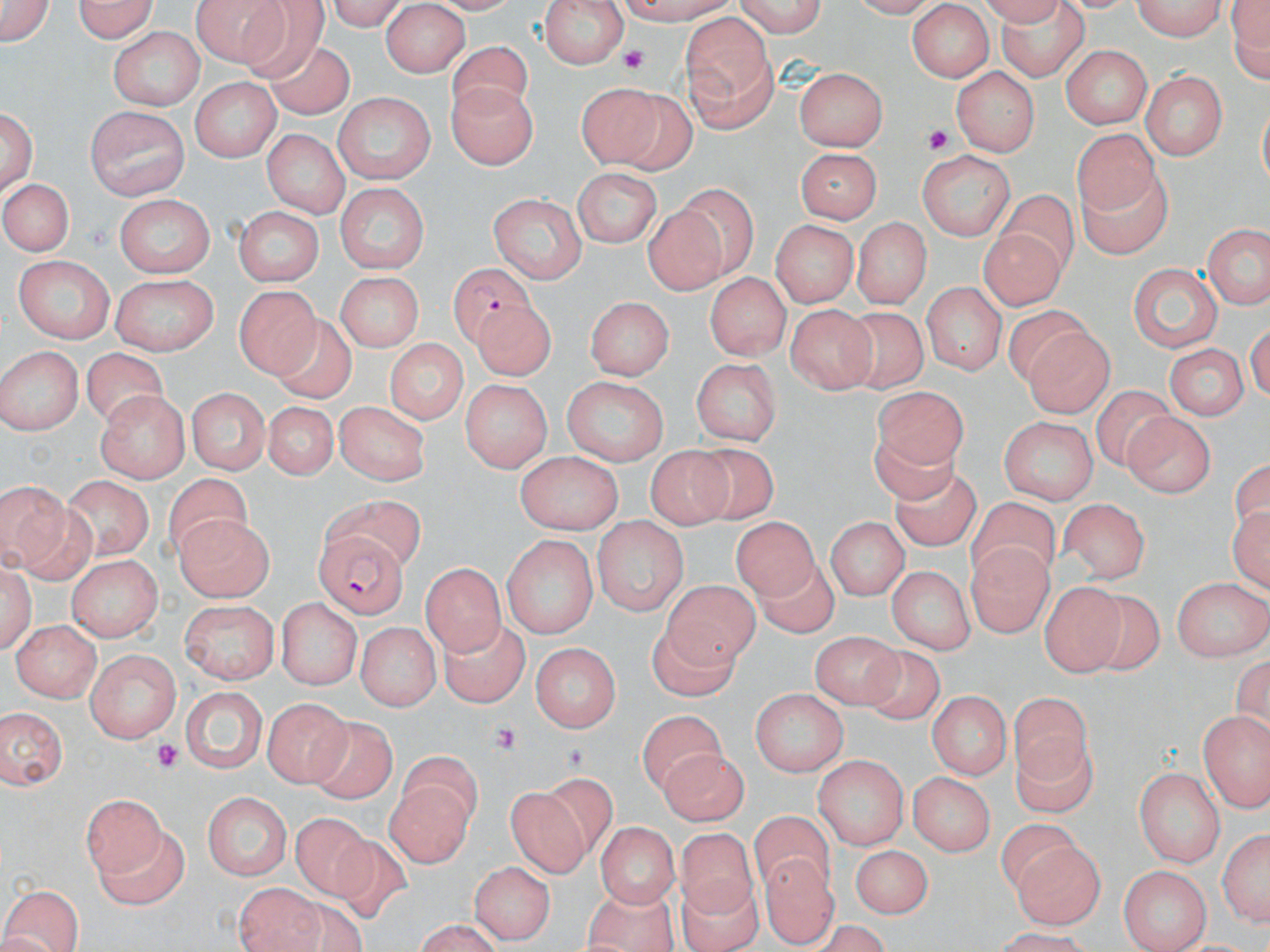 Approximate bounding boxes as [x1, y1, x2, y2] in pixels. Platelet locations: [617, 45, 659, 79], [918, 121, 953, 160], [484, 719, 520, 750], [149, 739, 186, 777]. Plasmodium falciparum-infected red blood cell locations: [440, 263, 546, 348], [316, 531, 410, 617]. Uninfected red blood cell locations: [71, 0, 160, 42], [192, 0, 297, 67], [730, 0, 830, 36], [1129, 0, 1229, 40], [1224, 0, 1269, 93], [541, 3, 625, 70], [1, 4, 56, 49], [991, 4, 1093, 88], [382, 5, 467, 75], [908, 5, 993, 80], [237, 7, 334, 91], [680, 16, 779, 136], [109, 28, 206, 110], [445, 43, 541, 121], [1059, 44, 1151, 130], [256, 46, 368, 127], [954, 66, 1037, 157], [797, 67, 889, 152], [1140, 69, 1226, 160], [191, 80, 278, 162], [448, 80, 535, 170], [576, 85, 667, 176], [448, 86, 539, 177], [330, 94, 436, 188], [616, 95, 708, 182], [1, 103, 39, 202], [87, 106, 187, 203], [1064, 125, 1174, 214], [263, 130, 350, 216], [796, 148, 879, 224], [919, 150, 1016, 238], [1070, 167, 1175, 264], [572, 168, 663, 249], [0, 175, 72, 260], [332, 184, 430, 273], [680, 188, 764, 273], [1002, 190, 1079, 282], [492, 195, 586, 282], [112, 196, 218, 273], [231, 208, 325, 286], [649, 209, 728, 296], [850, 216, 928, 310], [770, 220, 855, 308], [1203, 223, 1269, 313], [980, 229, 1064, 312], [14, 255, 116, 341], [1125, 265, 1222, 356], [706, 270, 790, 358], [337, 271, 424, 353], [112, 274, 216, 356], [922, 278, 1002, 378], [234, 285, 324, 378], [583, 294, 672, 382], [996, 302, 1089, 387], [787, 303, 876, 391], [838, 308, 934, 393], [469, 309, 559, 378], [266, 310, 359, 404], [1025, 328, 1117, 420], [383, 336, 470, 425], [1170, 341, 1248, 423], [0, 345, 82, 436], [78, 345, 171, 426], [689, 355, 785, 447], [563, 375, 668, 465], [462, 379, 549, 472], [871, 384, 973, 473], [184, 386, 272, 473], [1092, 388, 1186, 476], [100, 393, 189, 481], [259, 399, 346, 484], [335, 401, 425, 484], [1124, 411, 1213, 497], [999, 415, 1097, 503], [869, 433, 961, 510], [683, 442, 782, 522], [648, 446, 737, 533], [516, 448, 620, 531], [67, 474, 152, 561], [164, 474, 256, 569], [886, 474, 980, 553], [0, 481, 80, 578], [321, 497, 428, 562], [1059, 498, 1151, 579], [966, 499, 1061, 587], [733, 513, 819, 599], [173, 515, 277, 599], [824, 517, 907, 601], [594, 519, 688, 617], [501, 536, 596, 639], [965, 543, 1051, 636], [66, 555, 162, 642], [0, 560, 36, 659], [754, 561, 842, 639], [419, 562, 504, 655], [886, 564, 972, 655], [1167, 573, 1270, 656], [660, 577, 757, 667], [1039, 583, 1131, 672], [1097, 589, 1167, 674], [276, 597, 361, 689], [177, 601, 280, 686], [637, 616, 741, 704], [11, 618, 100, 702], [442, 619, 529, 705], [359, 620, 439, 707], [811, 631, 902, 706], [529, 640, 623, 733], [864, 647, 954, 727], [86, 650, 182, 743], [183, 686, 267, 773], [748, 689, 849, 776], [1010, 692, 1097, 788], [925, 693, 1010, 780], [265, 696, 350, 786], [1, 708, 70, 789], [639, 708, 729, 795], [1197, 709, 1270, 812], [305, 717, 398, 804], [1015, 732, 1099, 815], [657, 748, 744, 823], [813, 756, 907, 852], [390, 762, 481, 864], [1135, 767, 1225, 866], [910, 770, 998, 854], [508, 774, 610, 873], [202, 788, 291, 884], [84, 791, 166, 878], [289, 814, 382, 903], [750, 814, 835, 892], [595, 820, 677, 909], [1216, 823, 1270, 929], [89, 826, 186, 906], [679, 831, 760, 922], [1014, 841, 1104, 928], [854, 843, 936, 919], [764, 852, 837, 947], [472, 859, 553, 945], [1119, 861, 1210, 949], [680, 871, 764, 952], [2, 881, 84, 952], [235, 882, 317, 951], [580, 882, 676, 952], [406, 919, 503, 951]. Slide-level diagnosis: Plasmodium falciparum. Image is 1270×952 pixels. Optical microscopy. Thin blood smear. May-Grünwald-Giemsa-stained preparation. Captured at 1000x magnification. Single field of view.